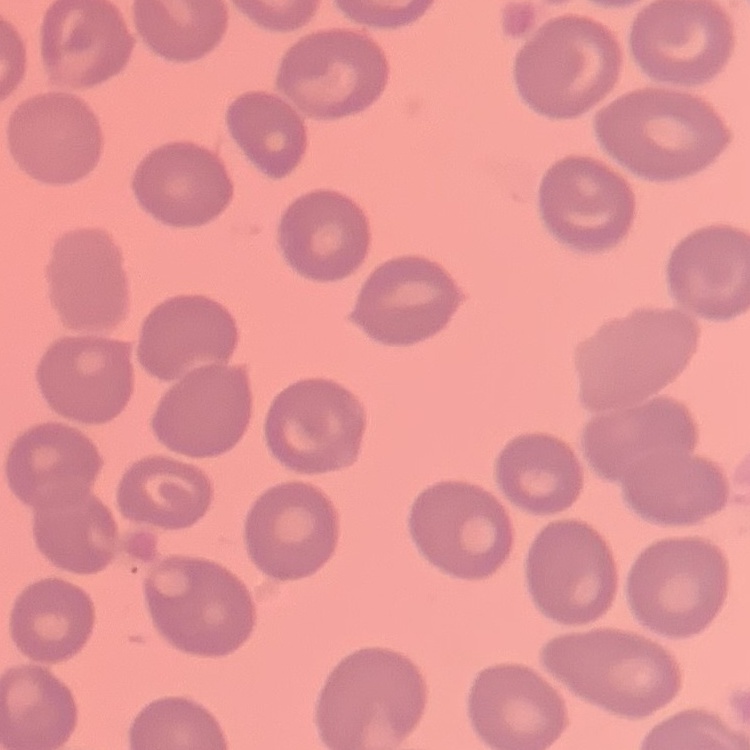
{
  "red_blood_cell_morphology": "no rouleaux formation",
  "preparation": "thin blood smear",
  "image_type": "one tile cut from a larger photomicrograph",
  "stain": "Field's or Giemsa"
}